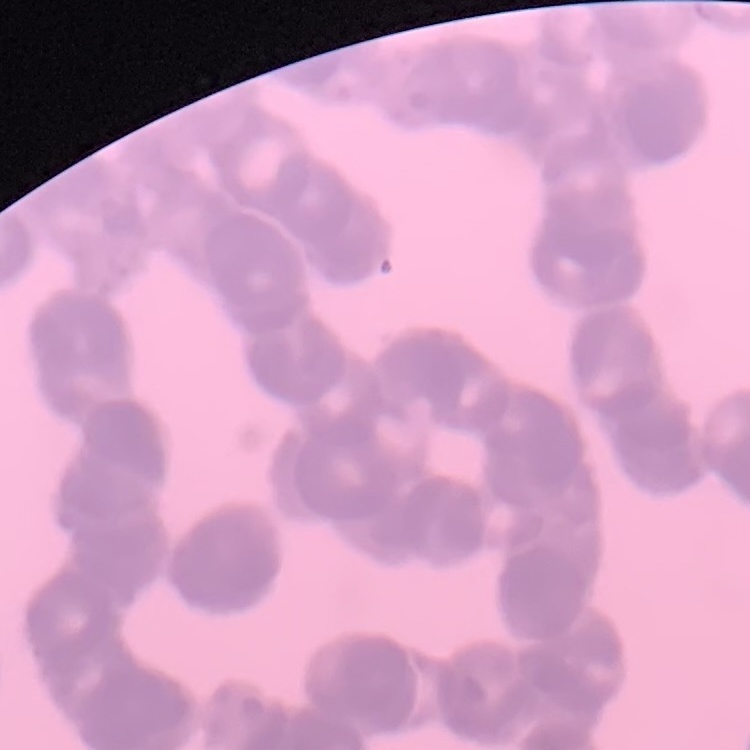
The red blood cells exhibit rouleaux formation. One tile cut from a larger photomicrograph. Thin blood smear. Stained with either Field's or Giemsa.